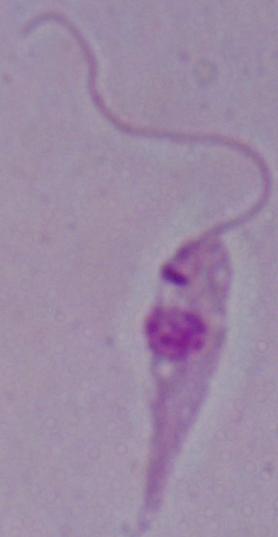

Summary:
  - Magnification: 1000x
  - Modality: photomicrograph
  - Identification: Leishmania